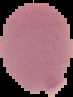

Summary:
  - Preparation: thin blood film
  - Image size: 73×97 pixels
  - Image type: segmented cell region on a black background
  - Result: no malaria parasites seen